Assess the morphology of the erythrocytes.
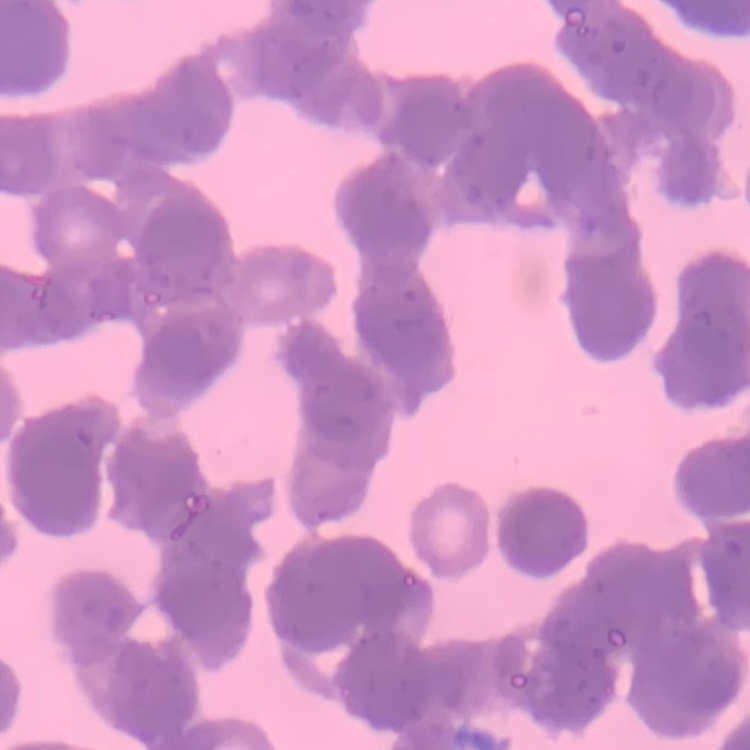
Rouleaux formation.

Stained with either Field's or Giemsa. Square crop of a larger photomicrograph. Thin blood film.